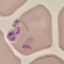

{
  "result": "malaria parasites detected",
  "capture": "smartphone through the microscope eyepiece",
  "stain": "Giemsa",
  "image_type": "cell patch, automatically extracted from a larger field of view and resized to 64 × 64 pixels",
  "preparation": "thin smear"
}